Identify the preparation type.
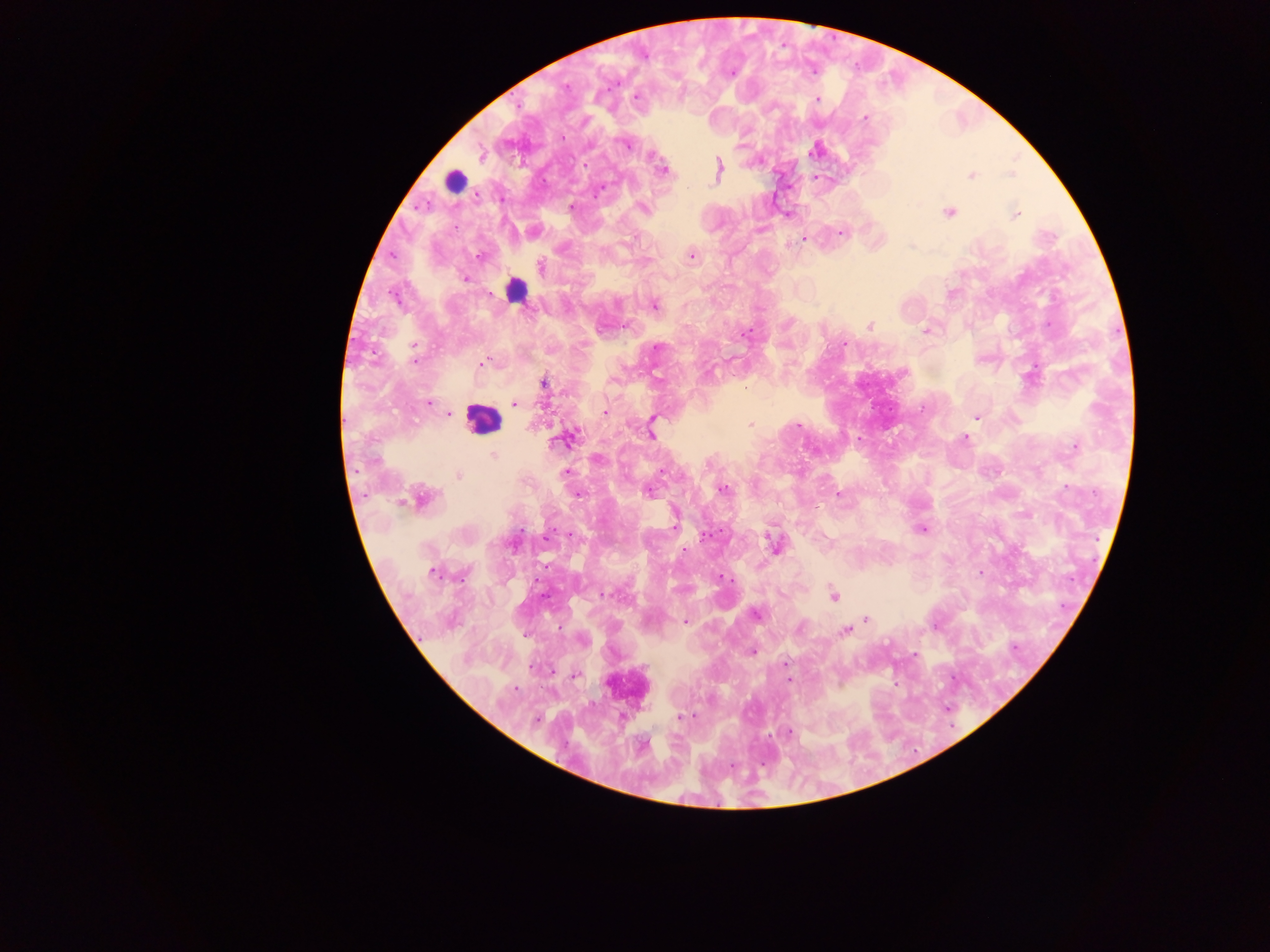

Thick blood smear.

country: Ghana
field_of_view: single
capture: mobile-phone photograph through a microscope
malaria_parasite_locations: 'approximate centers as (x, y) in pixels: (566, 87), (636, 98), (817, 100), (865, 118), (627, 145), (816, 150), (481, 156), (719, 168), (663, 170), (1011, 174), (971, 175), (598, 191), (571, 206), (643, 208), (949, 213), (1015, 214), (759, 229), (841, 232), (804, 240), (478, 256), (691, 256), (541, 267), (465, 279), (950, 293), (654, 305), (870, 326), (926, 331), (745, 334), (843, 344), (414, 346), (657, 347), (414, 362), (483, 363), (544, 383), (429, 403), (515, 404), (605, 412), (449, 414), (976, 417), (654, 418), (652, 424), (750, 424), (798, 426), (651, 435), (964, 438), (563, 439), (860, 440), (1074, 447), (493, 454), (662, 471), (565, 473), (458, 476), (1067, 486), (723, 490), (649, 492), (838, 493), (423, 498), (675, 523), (922, 529), (521, 530), (774, 545), (684, 550), (432, 573), (980, 573), (722, 577), (606, 594), (833, 595), (756, 614), (866, 618), (685, 621), (845, 631), (752, 651), (916, 655), (785, 663), (575, 675), (788, 679), (514, 689), (690, 715), (682, 716), (537, 719), (789, 731)'
image_size: 1270×952 pixels
leukocyte_locations: 'approximate centers as (x, y) in pixels: (463, 178), (515, 290), (481, 418)'